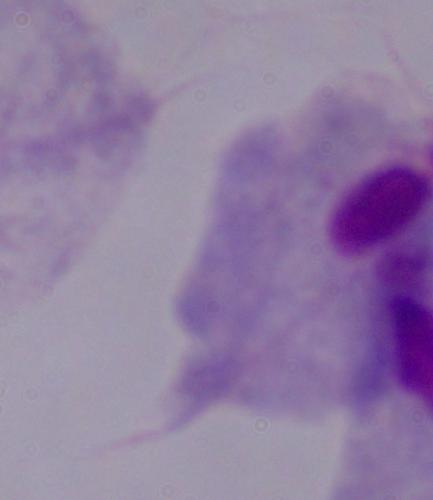
Photomicrograph. Captured at 1000x magnification. A trichomonad is shown.